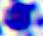
Summary:
  - Modality: photomicrograph
  - Magnification: 400x
  - Identification: white blood cell